Classify this cell by malaria status.
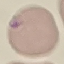

Parasitized.

Thin blood film. Giemsa-stained preparation. Automatically extracted cell patch, resized to 64 × 64 pixels. Photographed with a smartphone camera at the microscope eyepiece.